Outline each uninfected red blood cell.
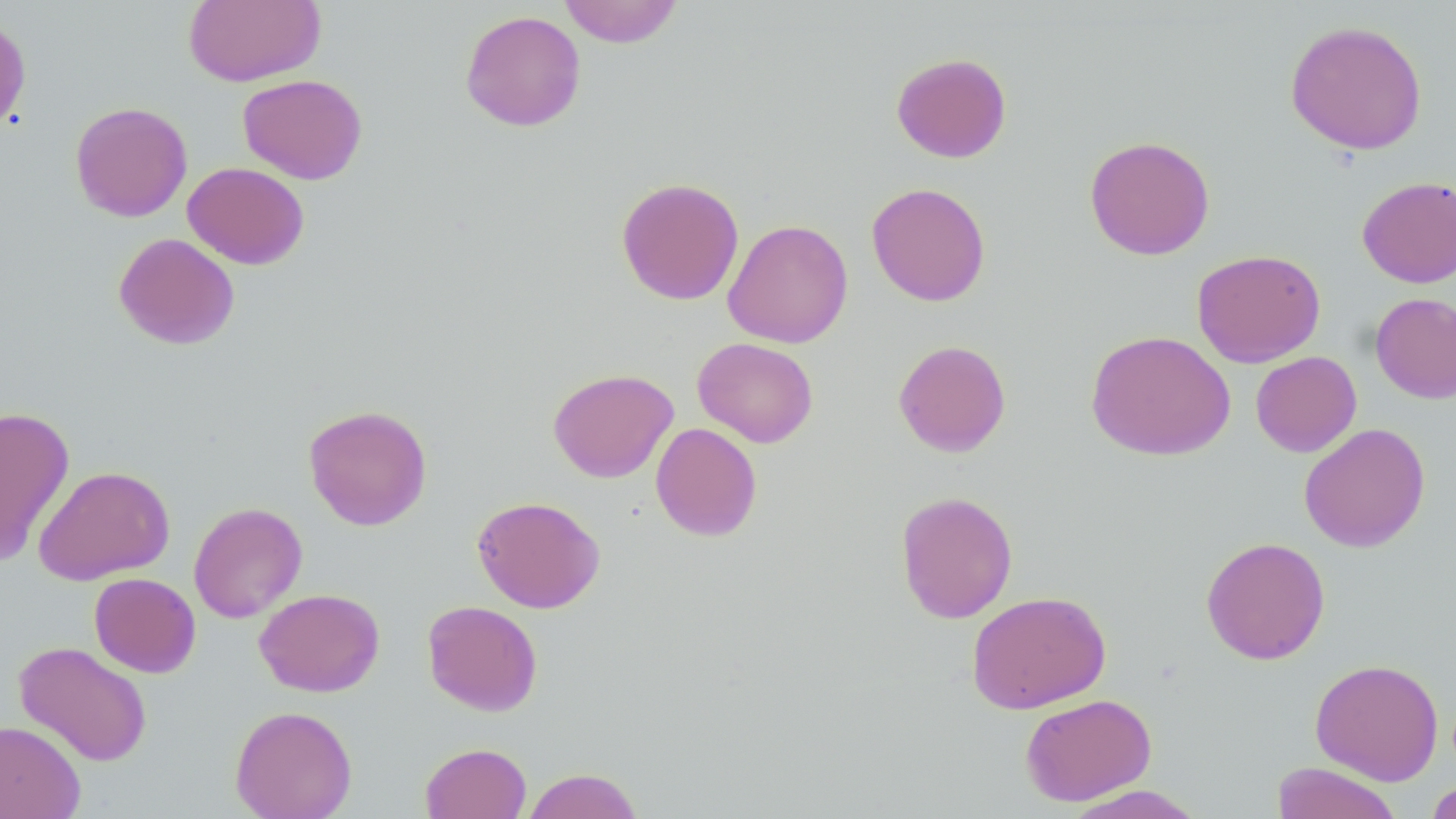

Approximate bounding boxes as (x1, y1, x2, y2) in pixels.
Uninfected red blood cells: (182, 0, 326, 87), (557, 0, 684, 48), (460, 9, 586, 132), (0, 13, 31, 136), (1285, 19, 1428, 155), (891, 52, 1012, 163), (237, 74, 368, 185), (70, 101, 193, 222), (1084, 135, 1215, 260), (182, 162, 310, 269), (1357, 176, 1456, 288), (616, 177, 745, 305), (866, 182, 991, 307), (723, 218, 853, 348), (113, 232, 240, 350), (1191, 248, 1326, 368), (1370, 292, 1456, 404), (1086, 329, 1236, 461), (692, 337, 819, 447), (893, 339, 1011, 457), (1251, 351, 1362, 457), (547, 367, 679, 483), (303, 404, 432, 531), (0, 406, 75, 566), (650, 422, 763, 542), (1299, 423, 1430, 552), (33, 465, 175, 585), (895, 490, 1018, 623), (472, 495, 605, 613), (188, 502, 307, 623), (1200, 536, 1331, 665), (89, 572, 201, 678), (254, 588, 385, 697), (966, 590, 1111, 714), (422, 600, 543, 716), (14, 641, 153, 766), (1309, 658, 1444, 785), (1020, 693, 1157, 806), (229, 704, 357, 819), (0, 721, 85, 819), (420, 742, 532, 819), (1271, 761, 1403, 819), (523, 767, 644, 818), (1425, 779, 1456, 819), (1061, 785, 1206, 818).

{
  "slide_level_diagnosis": "negative for blood parasites",
  "preparation": "thin blood smear",
  "field_of_view": "single",
  "modality": "optical microscopy",
  "magnification": "1000x",
  "stain": "May-Grünwald-Giemsa",
  "image_size": "1456×819 pixels"
}